Outline each Plasmodium ovale-infected red blood cell.
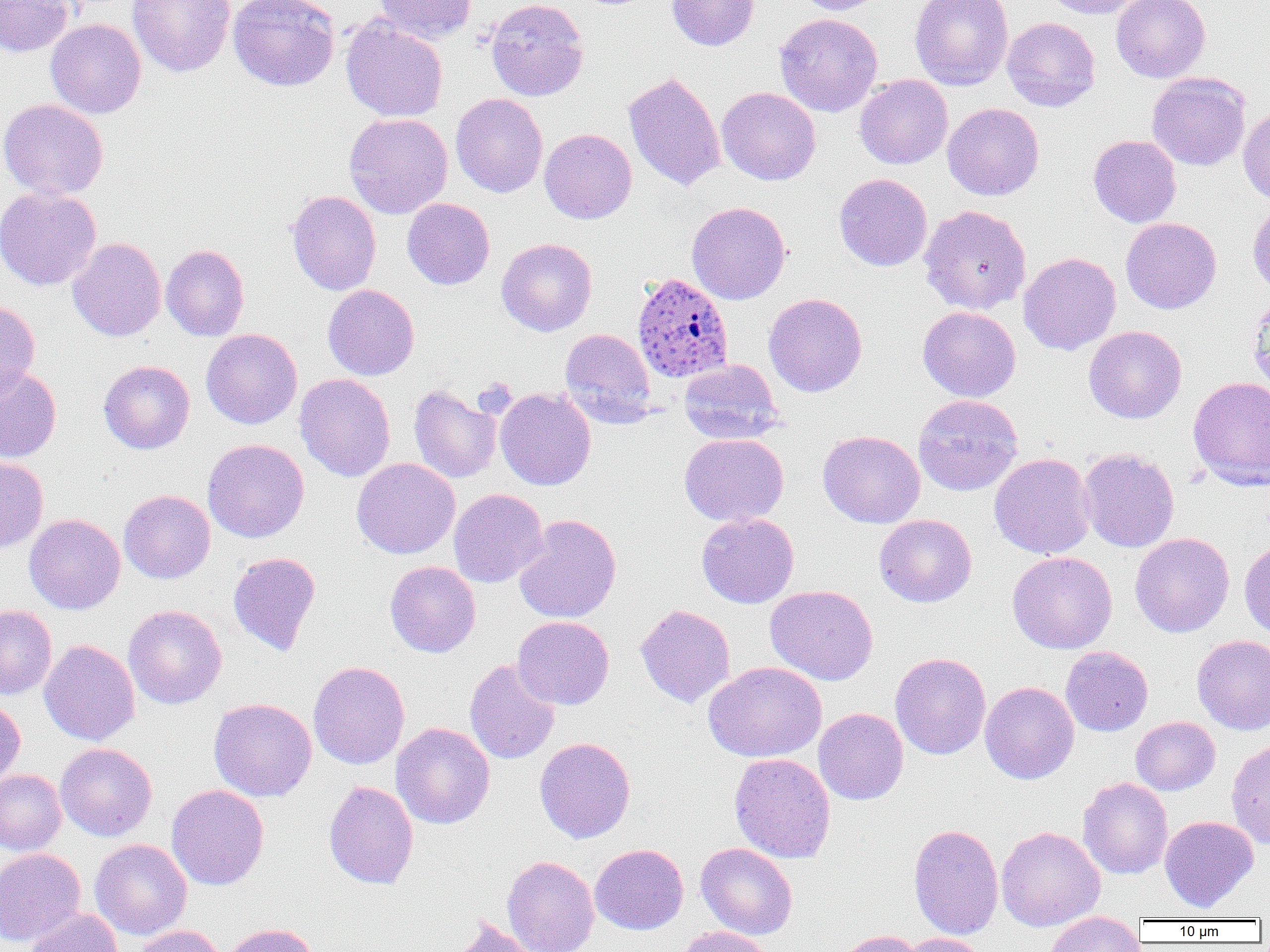
Approximate bounding boxes as (x1,y1)-(x2,y2) corner pairs in pixels.
Plasmodium ovale-infected red blood cells: (632,272)-(733,384).

Uninfected red blood cell locations: (0,0)-(73,56), (128,0)-(236,77), (228,0)-(340,91), (374,0)-(478,43), (486,0)-(588,101), (666,0)-(759,51), (796,0)-(889,15), (910,0)-(1013,90), (1038,0)-(1149,19), (1111,0)-(1210,83), (774,13)-(883,116), (341,16)-(448,122), (1002,17)-(1100,112), (45,19)-(146,119), (623,70)-(726,192), (1147,72)-(1250,171), (854,74)-(953,169), (717,87)-(821,185), (450,93)-(547,197), (0,99)-(109,199), (942,103)-(1044,201), (1238,106)-(1270,205), (344,113)-(453,219), (539,128)-(637,224), (1088,134)-(1182,228), (834,173)-(932,271), (0,186)-(101,291), (287,190)-(381,295), (402,198)-(495,290), (1247,198)-(1270,295), (686,201)-(790,305), (919,205)-(1031,314), (1121,217)-(1221,314), (497,237)-(597,336), (68,238)-(166,341), (161,244)-(249,341), (1019,252)-(1121,355), (323,284)-(419,380), (764,292)-(868,397), (1247,294)-(1270,398), (0,300)-(40,398), (918,306)-(1021,402), (1084,325)-(1186,423), (201,328)-(302,429), (560,328)-(656,424), (679,358)-(785,444), (98,360)-(195,454), (0,363)-(62,463), (294,373)-(396,481), (1188,376)-(1270,490), (408,385)-(501,483), (495,388)-(596,490), (913,394)-(1023,495), (818,430)-(925,528), (679,433)-(789,526), (202,439)-(309,543), (1078,448)-(1180,552), (989,453)-(1095,559), (0,455)-(48,553), (352,458)-(460,559), (118,489)-(215,583), (449,489)-(548,588), (24,513)-(126,614), (696,513)-(799,608), (513,514)-(621,623), (874,514)-(977,607), (1130,532)-(1234,637), (1239,538)-(1270,641), (228,551)-(321,656), (1008,551)-(1117,653), (384,561)-(481,657), (765,585)-(878,685), (635,604)-(735,708), (0,605)-(57,700), (123,605)-(227,709), (513,616)-(614,709), (1192,635)-(1270,734), (39,640)-(140,745), (1060,646)-(1153,736), (890,652)-(991,759), (464,658)-(560,764), (308,660)-(410,769), (704,661)-(826,762), (980,681)-(1079,784), (0,697)-(25,788), (209,698)-(317,801), (814,708)-(908,805), (1131,716)-(1220,795), (391,722)-(495,829), (534,737)-(636,843), (1225,738)-(1270,849), (55,743)-(157,841), (729,753)-(836,863), (0,769)-(66,854), (1078,777)-(1173,879), (323,780)-(419,889), (167,784)-(269,891), (1159,815)-(1259,912), (908,823)-(1004,940), (995,825)-(1105,932), (90,839)-(192,940), (695,842)-(798,940), (590,843)-(689,935), (0,848)-(86,945), (502,855)-(599,952), (25,907)-(123,952), (1044,912)-(1145,952), (449,917)-(539,952), (221,923)-(318,952), (132,925)-(225,952), (674,926)-(773,952), (831,929)-(922,952), (896,933)-(989,952). Slide-level diagnosis: Plasmodium ovale. Single field of view. Thin blood film. Light microscopy. Image is 1270×952 pixels. 1000x magnification.